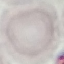 Malaria status: uninfected. Giemsa-stained preparation. Thin blood smear. Acquired by smartphone through the microscope eyepiece. Automatically extracted cell patch, resized to 64 × 64 pixels.